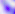
Summary:
  - Magnification: 400x
  - Identification: Toxoplasma gondii
  - Modality: photomicrograph